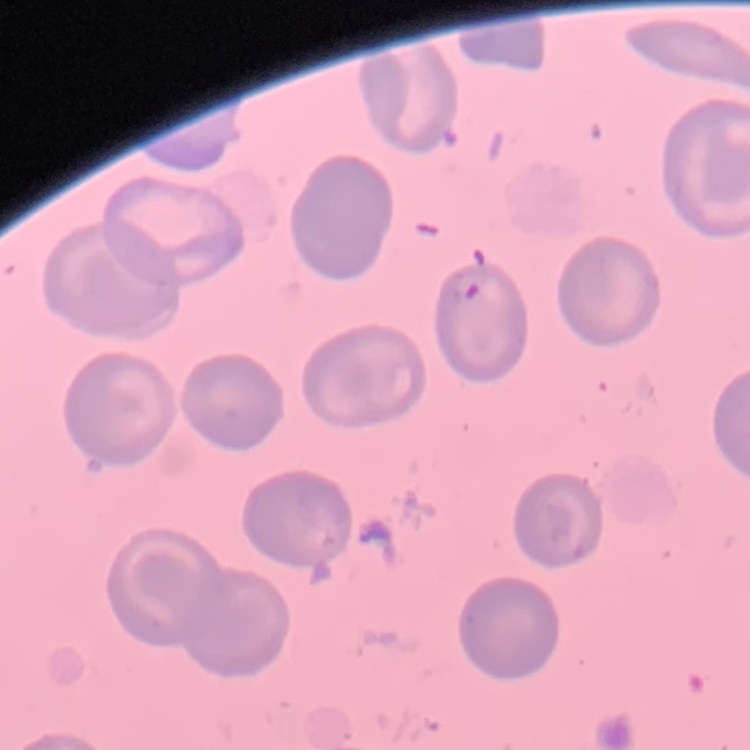 The erythrocytes exhibit no rouleaux formation. Stained with either Field's or Giemsa. Thin blood film. One tile cut from a larger photomicrograph.